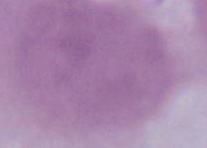

Summary:
  - Modality: photomicrograph
  - Magnification: 1000x
  - Identification: erythrocyte